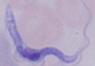
Summary:
  - Identification: trypanosome
  - Magnification: 1000x
  - Modality: micrograph